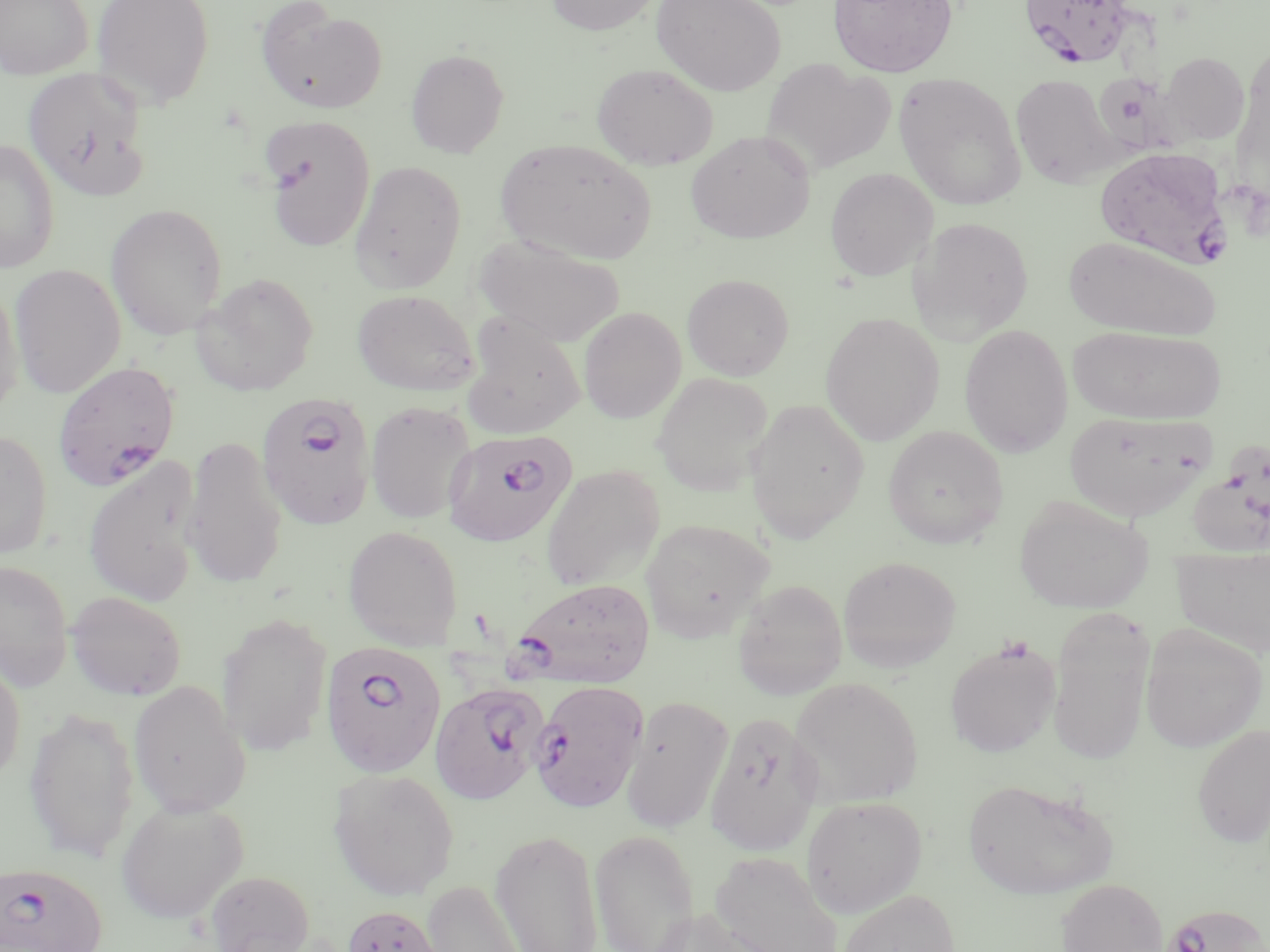
Summary:
  - Coordinate format: approximate bounding boxes as named x1/y1/x2/y2 corners in pixels
  - Uninfected red blood cell locations: (x1=0, y1=0, x2=93, y2=79), (x1=91, y1=0, x2=215, y2=109), (x1=545, y1=0, x2=662, y2=36), (x1=652, y1=0, x2=786, y2=97), (x1=828, y1=0, x2=958, y2=78), (x1=255, y1=2, x2=389, y2=115), (x1=406, y1=48, x2=509, y2=158), (x1=1161, y1=52, x2=1250, y2=144), (x1=761, y1=59, x2=895, y2=176), (x1=591, y1=62, x2=719, y2=171), (x1=23, y1=67, x2=151, y2=200), (x1=894, y1=72, x2=1027, y2=211), (x1=1011, y1=73, x2=1119, y2=189), (x1=260, y1=116, x2=376, y2=252), (x1=685, y1=130, x2=815, y2=244), (x1=0, y1=138, x2=60, y2=273), (x1=495, y1=138, x2=659, y2=265), (x1=349, y1=160, x2=467, y2=294), (x1=825, y1=167, x2=938, y2=281), (x1=105, y1=203, x2=228, y2=339), (x1=908, y1=216, x2=1034, y2=343), (x1=474, y1=234, x2=625, y2=347), (x1=1064, y1=236, x2=1220, y2=341), (x1=9, y1=264, x2=126, y2=398), (x1=192, y1=273, x2=319, y2=396), (x1=682, y1=274, x2=794, y2=380), (x1=0, y1=278, x2=25, y2=417), (x1=352, y1=289, x2=479, y2=396), (x1=579, y1=307, x2=686, y2=424), (x1=821, y1=312, x2=944, y2=445), (x1=461, y1=315, x2=586, y2=440), (x1=958, y1=324, x2=1073, y2=457), (x1=1068, y1=325, x2=1225, y2=425), (x1=652, y1=372, x2=773, y2=496), (x1=746, y1=398, x2=869, y2=543), (x1=366, y1=401, x2=475, y2=524), (x1=1064, y1=409, x2=1215, y2=521), (x1=883, y1=425, x2=1009, y2=549), (x1=0, y1=428, x2=52, y2=559), (x1=1184, y1=434, x2=1270, y2=559), (x1=181, y1=435, x2=288, y2=589), (x1=83, y1=455, x2=204, y2=607), (x1=541, y1=464, x2=665, y2=592), (x1=1014, y1=495, x2=1153, y2=614), (x1=641, y1=518, x2=773, y2=643), (x1=343, y1=525, x2=463, y2=649), (x1=1171, y1=545, x2=1270, y2=656), (x1=839, y1=556, x2=961, y2=673), (x1=0, y1=559, x2=73, y2=691), (x1=732, y1=579, x2=847, y2=699), (x1=66, y1=591, x2=187, y2=701), (x1=1047, y1=608, x2=1154, y2=766), (x1=216, y1=612, x2=333, y2=756), (x1=1140, y1=624, x2=1266, y2=753), (x1=944, y1=639, x2=1060, y2=758), (x1=0, y1=654, x2=26, y2=788), (x1=790, y1=677, x2=923, y2=807), (x1=128, y1=680, x2=251, y2=818), (x1=621, y1=696, x2=733, y2=833), (x1=23, y1=705, x2=139, y2=864), (x1=704, y1=711, x2=823, y2=856), (x1=1192, y1=723, x2=1270, y2=848), (x1=328, y1=768, x2=459, y2=901), (x1=963, y1=777, x2=1117, y2=901), (x1=801, y1=795, x2=927, y2=917), (x1=115, y1=799, x2=249, y2=924), (x1=490, y1=828, x2=603, y2=951), (x1=589, y1=830, x2=701, y2=951), (x1=710, y1=851, x2=843, y2=952), (x1=204, y1=870, x2=315, y2=952), (x1=1056, y1=878, x2=1168, y2=952), (x1=421, y1=879, x2=531, y2=952), (x1=836, y1=889, x2=962, y2=952), (x1=340, y1=903, x2=450, y2=952), (x1=644, y1=907, x2=781, y2=952)
  - Plasmodium falciparum-infected red blood cell locations: (x1=1019, y1=0, x2=1138, y2=68), (x1=1094, y1=146, x2=1231, y2=267), (x1=52, y1=361, x2=180, y2=491), (x1=255, y1=392, x2=377, y2=529), (x1=444, y1=429, x2=576, y2=547), (x1=511, y1=577, x2=656, y2=687), (x1=321, y1=642, x2=448, y2=779), (x1=530, y1=680, x2=649, y2=812), (x1=430, y1=681, x2=547, y2=804), (x1=1, y1=865, x2=107, y2=952), (x1=1161, y1=902, x2=1266, y2=952)
  - Slide-level diagnosis: Plasmodium falciparum
  - Preparation: thin blood smear
  - Modality: optical microscopy
  - Magnification: 1000x
  - Field of view: one of a larger specimen
  - Image size: 1270×952 pixels
  - Stain: May-Grünwald-Giemsa